Classify this cell by malaria status.
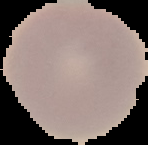

It is uninfected.

preparation: thin blood film
image_size: 148×145 pixels
image_type: segmented cell region with the area outside set to black